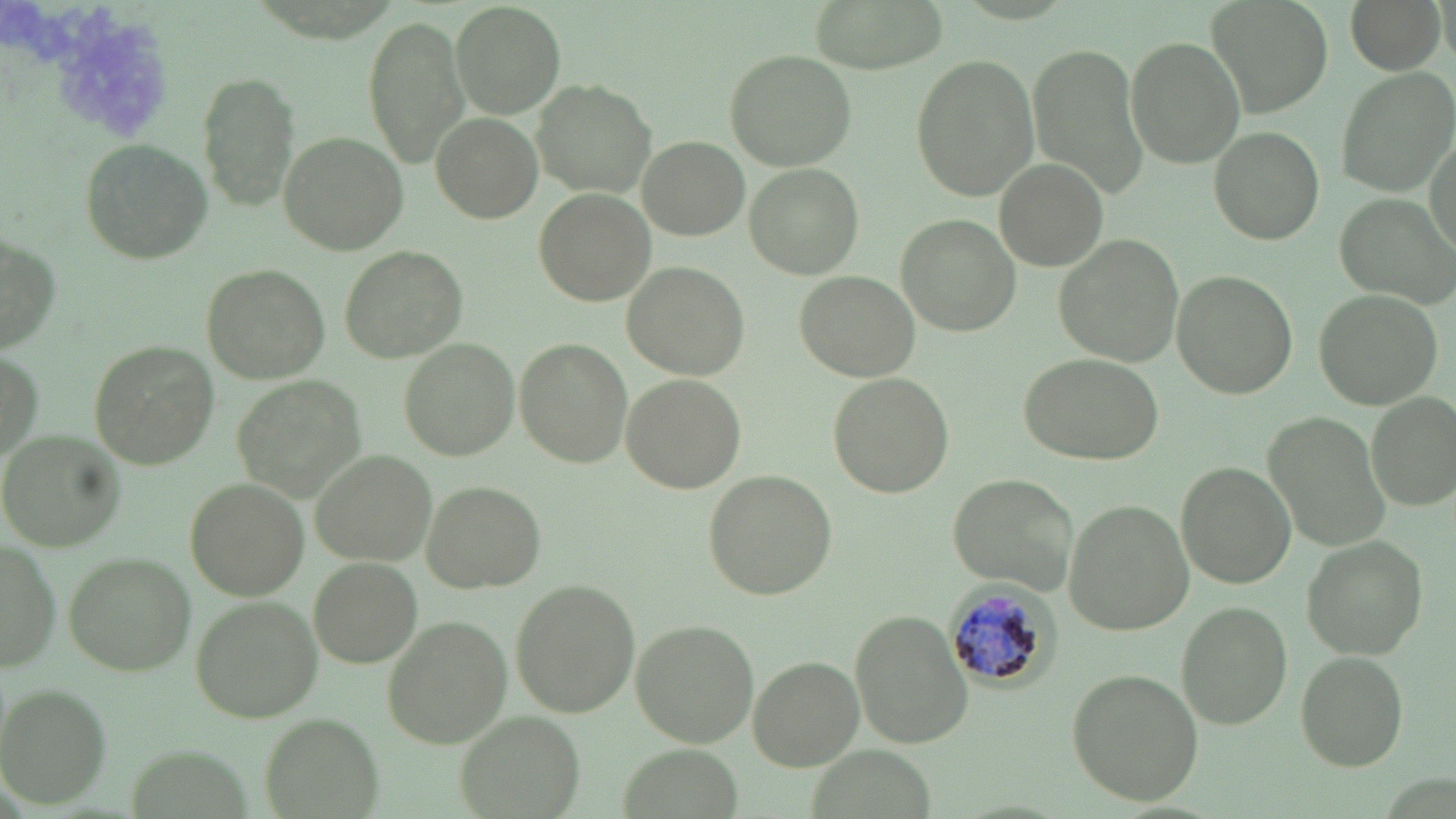
Summary:
  - Coordinate format: approximate bounding boxes as [x1, y1, x2, y2] in pixels
  - Plasmodium malariae-infected red blood cell locations: [943, 580, 1058, 695]
  - Uninfected red blood cell locations: [811, 0, 950, 71], [1209, 0, 1331, 113], [1347, 0, 1446, 72], [450, 2, 565, 116], [363, 16, 471, 167], [1125, 36, 1247, 168], [1028, 43, 1150, 197], [724, 48, 857, 170], [909, 54, 1040, 201], [1334, 67, 1456, 194], [199, 70, 297, 212], [532, 80, 657, 197], [431, 112, 541, 222], [1426, 125, 1456, 265], [1209, 127, 1325, 244], [277, 131, 407, 256], [638, 136, 747, 239], [81, 140, 213, 260], [998, 161, 1106, 269], [743, 164, 863, 279], [535, 188, 657, 304], [1335, 193, 1454, 305], [896, 216, 1020, 335], [1, 231, 62, 354], [1054, 234, 1188, 367], [341, 245, 467, 364], [623, 262, 751, 381], [204, 265, 330, 383], [1169, 269, 1297, 399], [795, 271, 921, 381], [1312, 289, 1441, 408], [515, 337, 631, 469], [401, 340, 520, 460], [88, 341, 219, 470], [1014, 353, 1166, 467], [828, 372, 953, 498], [235, 374, 365, 493], [621, 374, 744, 494], [1366, 392, 1455, 510], [1267, 411, 1389, 556], [1, 430, 123, 552], [313, 449, 436, 564], [1175, 462, 1297, 588], [703, 470, 837, 598], [947, 473, 1079, 594], [185, 479, 306, 599], [422, 481, 547, 593], [1064, 500, 1194, 634], [1303, 537, 1427, 658], [1, 538, 60, 673], [63, 554, 195, 675], [308, 558, 422, 668], [509, 580, 639, 717], [190, 596, 323, 723], [1175, 602, 1293, 729], [851, 611, 972, 748], [382, 617, 512, 748], [630, 620, 760, 746], [1296, 652, 1408, 769], [748, 656, 865, 768], [1068, 668, 1204, 806], [0, 686, 112, 808], [458, 710, 584, 818], [258, 713, 382, 819]
  - Slide-level diagnosis: Plasmodium malariae
  - Stain: May-Grünwald-Giemsa
  - Magnification: 1000x
  - Field of view: single
  - Modality: light microscopy
  - Preparation: thin blood smear
  - Image size: 1456×819 pixels